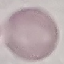

Summary:
  - Result: negative for malaria parasites
  - Image type: cell patch, automatically extracted from a larger field of view and resized to 64 × 64 pixels
  - Capture: smartphone through the microscope eyepiece
  - Preparation: thin smear
  - Stain: Giemsa